Comment on the morphology of the erythrocytes.
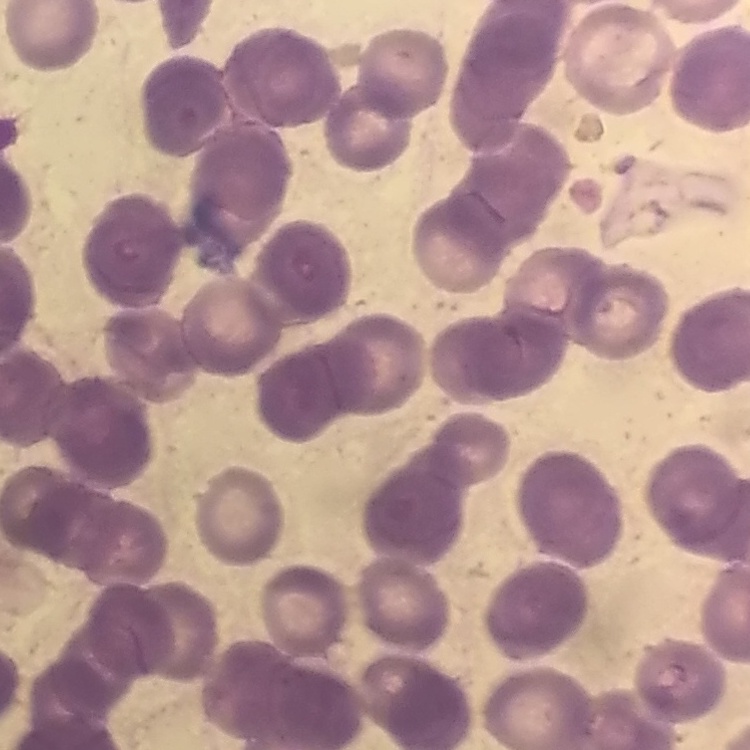
They show rouleaux formation.

Stained with either Field's or Giemsa. Thin peripheral smear. Square crop of a larger photomicrograph.